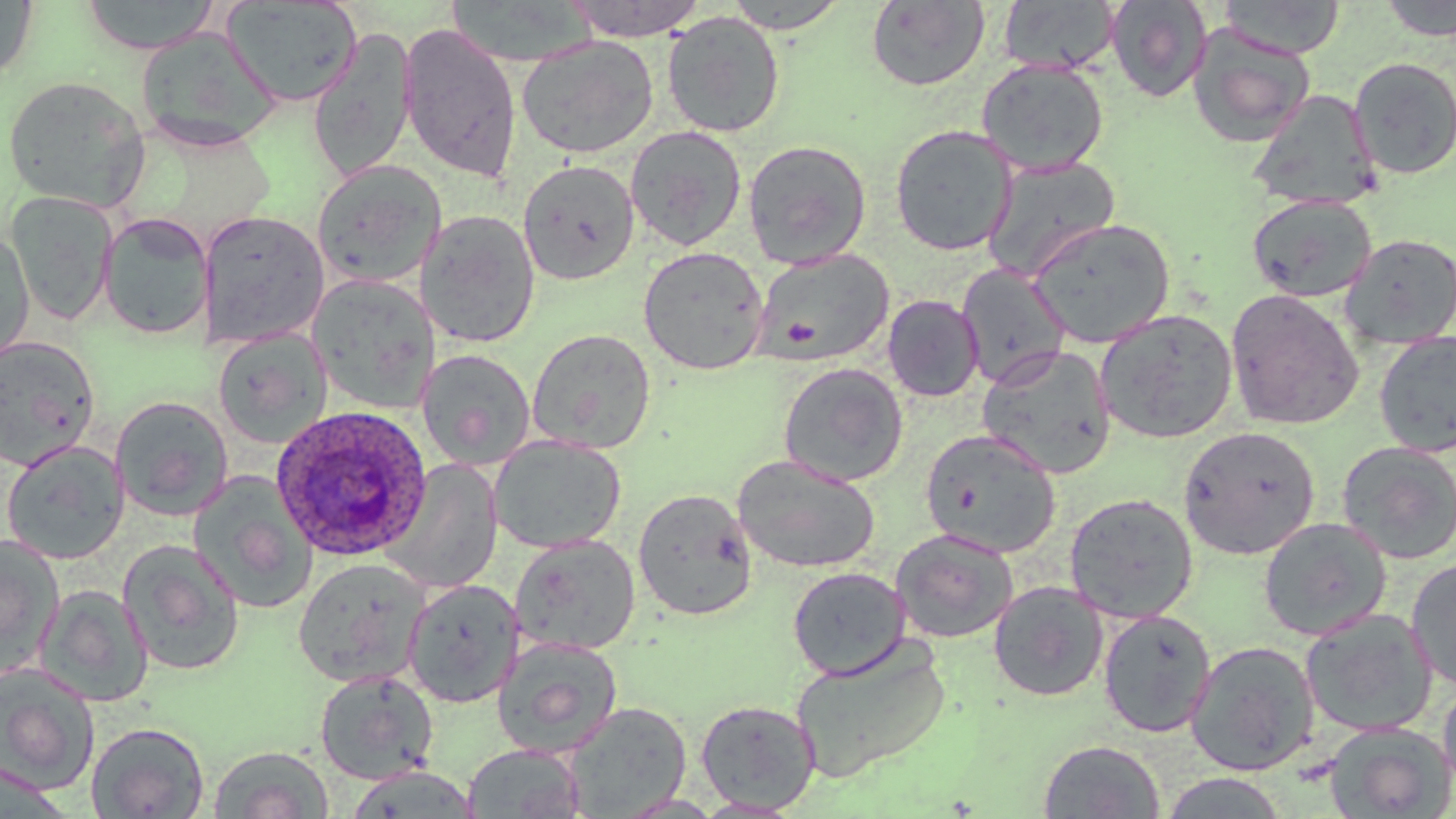

Approximate bounding boxes as (x1,y1)-(x2,y2) corner pairs in pixels. Plasmodium ovale-infected red blood cell locations: (270,404)-(433,561). Uninfected red blood cell locations: (80,0)-(222,54), (563,0)-(709,40), (723,0)-(849,33), (866,0)-(990,92), (998,0)-(1120,75), (1104,0)-(1212,103), (1219,0)-(1346,58), (1379,0)-(1455,41), (0,1)-(37,84), (223,1)-(363,106), (443,2)-(596,66), (662,11)-(786,138), (397,22)-(523,182), (1187,25)-(1315,147), (307,27)-(419,182), (135,28)-(281,152), (516,34)-(659,158), (1349,56)-(1456,180), (977,58)-(1109,176), (1,75)-(152,211), (1248,89)-(1381,211), (889,124)-(1018,256), (625,126)-(747,251), (742,139)-(872,269), (982,157)-(1121,281), (312,159)-(447,287), (518,159)-(639,285), (4,191)-(118,326), (1247,194)-(1378,303), (416,209)-(542,347), (198,210)-(330,347), (98,212)-(213,341), (1028,218)-(1176,348), (0,228)-(36,367), (1339,233)-(1456,350), (638,246)-(770,375), (752,248)-(895,367), (957,264)-(1071,388), (308,274)-(437,412), (1225,288)-(1364,431), (883,295)-(984,402), (1094,309)-(1237,444), (212,328)-(332,449), (527,328)-(656,454), (1374,331)-(1456,457), (0,336)-(101,469), (978,345)-(1117,479), (420,349)-(536,469), (778,362)-(908,486), (110,395)-(233,521), (1178,426)-(1320,560), (920,429)-(1061,558), (489,434)-(625,553), (1,440)-(130,564), (1337,441)-(1456,564), (732,454)-(880,574), (383,461)-(503,594), (188,471)-(319,614), (633,488)-(757,621), (1064,492)-(1199,622), (1258,516)-(1391,641), (890,528)-(1019,643), (510,533)-(641,655), (0,534)-(64,680), (117,539)-(245,677), (1406,556)-(1456,692), (294,558)-(430,687), (787,566)-(910,680), (402,578)-(524,707), (988,581)-(1108,702), (35,584)-(153,706), (1097,608)-(1216,738), (1299,608)-(1439,737), (493,637)-(623,757), (789,637)-(952,781), (1185,640)-(1321,776), (0,663)-(100,795), (314,669)-(439,784), (1437,679)-(1456,797), (695,699)-(820,814), (564,702)-(691,817), (86,721)-(210,818), (1323,722)-(1455,819), (1038,739)-(1165,818), (462,743)-(587,818), (208,745)-(333,819), (344,765)-(482,818), (1157,772)-(1290,818). Slide-level diagnosis: Plasmodium ovale. Image is 1456×819 pixels. 1000x magnification. Thin blood smear. May-Grünwald-Giemsa stain. Light microscopy. Single field of view.